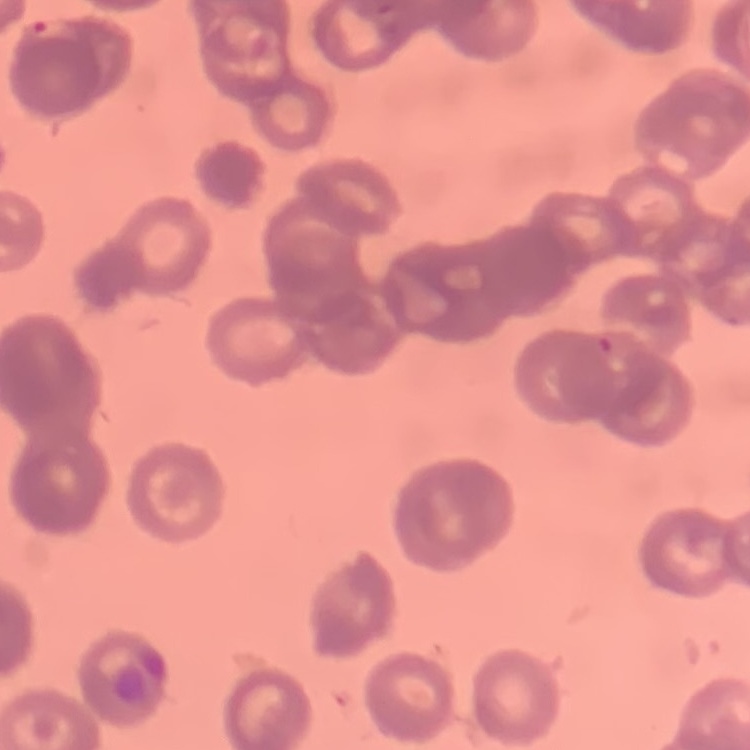 The red blood cells show rouleaux formation. One tile cut from a larger photomicrograph. Thin blood smear. Stained with either Field's or Giemsa.